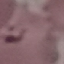 Result: malaria parasites detected. Giemsa-stained preparation. Thin blood film. Cell patch, automatically extracted from a larger field of view and resized to 64 × 64 pixels. Photographed with a smartphone camera at the microscope eyepiece.